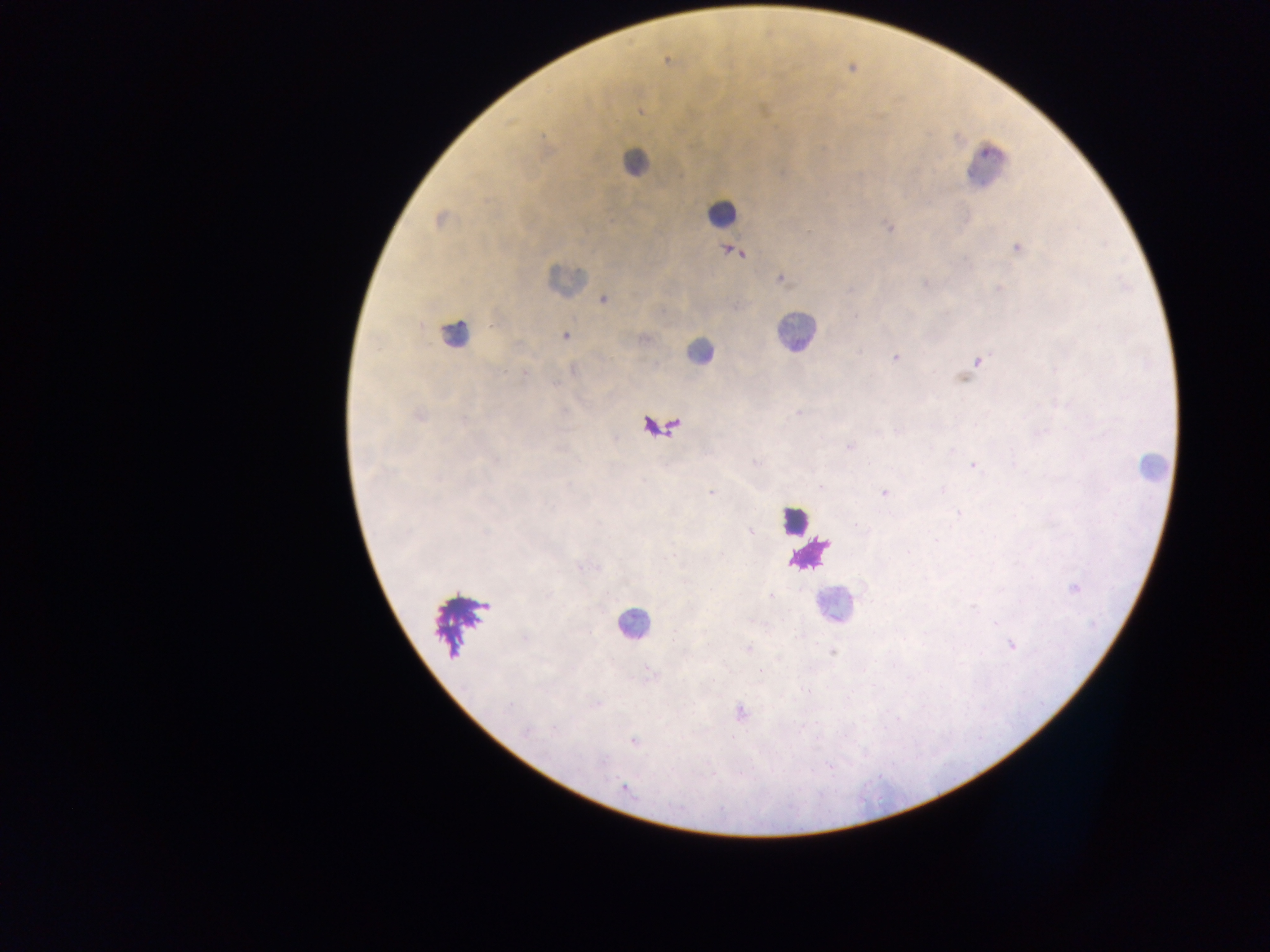 Approximate centers as (x, y) in pixels. Leukocyte locations: (635, 162), (985, 166), (721, 213), (565, 278), (795, 332), (454, 334), (699, 352), (661, 426), (1150, 468), (794, 520), (810, 553), (834, 606), (633, 626). Plasmodium parasite locations: (667, 61), (852, 69), (640, 111), (440, 219), (889, 227), (1017, 248), (732, 250), (780, 279), (925, 283), (999, 289), (604, 299), (566, 335), (896, 357), (978, 361), (418, 414), (849, 447), (973, 465), (821, 487), (710, 492), (885, 493), (1075, 587), (1011, 645), (833, 653), (740, 711), (633, 741), (624, 788). Single field of view. Photographed through a microscope with a mobile-phone camera. Image is 1270×952 pixels. Collected in Ghana. Thick blood film.